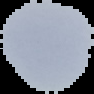
image_type: segmented cell region on a black background
image_size: 94×94 pixels
preparation: thin blood film
malaria_status: uninfected